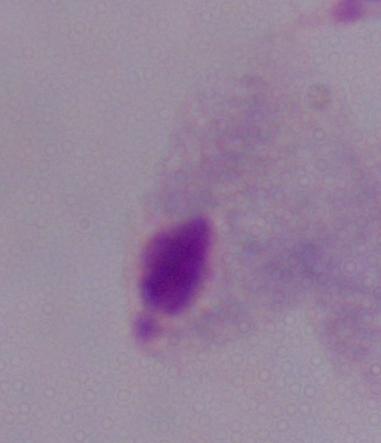

Summary:
  - Magnification: 1000x
  - Modality: photomicrograph
  - Identification: trichomonad